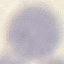

Summary:
  - Malaria status: uninfected
  - Preparation: thin blood film
  - Image type: cell patch, automatically extracted from a larger field of view and resized to 64 × 64 pixels
  - Stain: Giemsa
  - Capture: smartphone through the microscope eyepiece